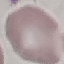 Result: no malaria parasites seen. Cell patch, automatically extracted from a larger field of view and resized to 64 × 64 pixels. Photographed with a smartphone camera at the microscope eyepiece. Thin blood film. Giemsa-stained preparation.